Describe the morphology of the red blood cells.
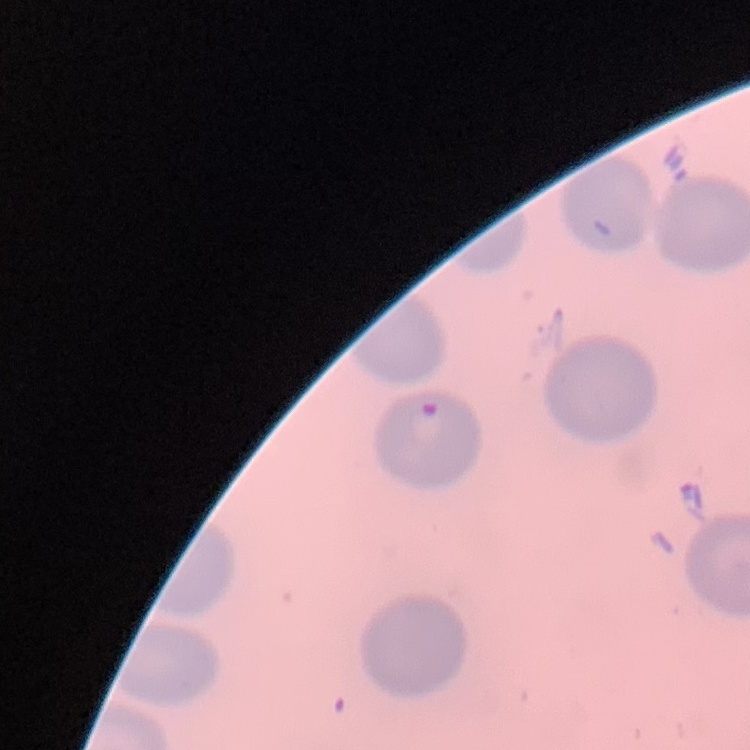
They show no rouleaux formation.

image type = square crop of a larger photomicrograph
preparation = thin blood film
stain = Field's or Giemsa